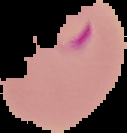

result = malaria parasites identified
preparation = thin blood film
image type = cell region segmented out of the field of view; surrounding area masked to black
image size = 127×133 pixels